Assess this cell for malaria.
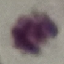
It is uninfected.

Summary:
  - Preparation: thin blood film
  - Stain: Giemsa
  - Image type: cell patch, automatically extracted from a larger field of view and resized to 64 × 64 pixels
  - Capture: smartphone through the microscope eyepiece